Outline each Plasmodium ovale-infected red blood cell.
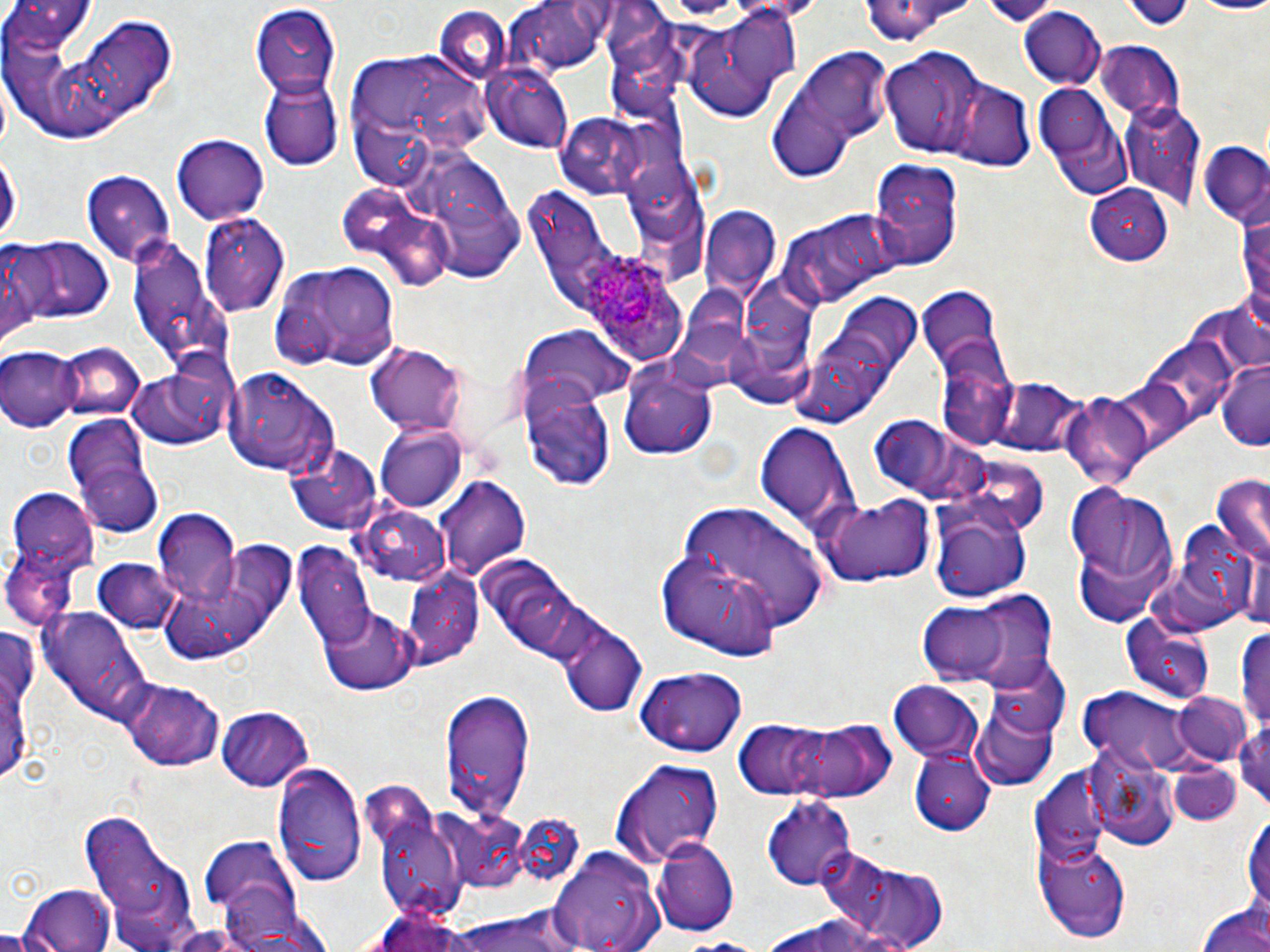
Approximate bounding boxes as (x1, y1, x2, y2) in pixels.
Plasmodium ovale-infected red blood cells: (584, 254, 676, 342).

{
  "slide_level_diagnosis": "Plasmodium ovale",
  "stain": "May-Grünwald-Giemsa",
  "modality": "optical microscopy",
  "field_of_view": "single",
  "preparation": "thin blood smear",
  "uninfected_red_blood_cell_locations": "approximate bounding boxes as (x1, y1, x2, y2) in pixels: (4, 0, 97, 66), (1181, 0, 1270, 16), (858, 1, 977, 44), (510, 2, 614, 76), (247, 4, 340, 97), (434, 6, 510, 86), (677, 8, 806, 121), (1017, 9, 1108, 88), (69, 12, 179, 125), (1095, 42, 1183, 123), (766, 45, 894, 180), (882, 47, 993, 159), (340, 50, 495, 185), (484, 67, 573, 154), (258, 73, 341, 169), (1034, 79, 1131, 196), (949, 80, 1035, 171), (1121, 103, 1206, 208), (554, 111, 654, 200), (169, 134, 271, 223), (1199, 144, 1269, 226), (0, 151, 19, 249), (417, 152, 528, 287), (869, 160, 965, 270), (82, 169, 176, 267), (337, 183, 418, 257), (1087, 184, 1175, 265), (1237, 203, 1270, 324), (700, 204, 781, 299), (777, 207, 899, 309), (200, 212, 290, 318), (382, 212, 456, 293), (126, 234, 230, 371), (20, 237, 113, 325), (1, 240, 51, 340), (275, 259, 402, 371), (917, 286, 1006, 381), (835, 291, 921, 373), (520, 328, 635, 412), (57, 341, 146, 423), (368, 342, 468, 437), (1, 345, 80, 431), (934, 350, 1018, 447), (616, 358, 719, 462), (122, 361, 231, 452), (1216, 362, 1270, 452), (226, 366, 340, 479), (986, 374, 1089, 458), (518, 376, 618, 491), (1059, 391, 1157, 489), (61, 413, 153, 513), (755, 422, 860, 534), (374, 425, 466, 513), (284, 440, 384, 535), (72, 448, 163, 537), (1209, 474, 1270, 568), (437, 475, 530, 579), (1066, 480, 1182, 624), (9, 490, 97, 569), (813, 495, 936, 587), (929, 500, 1034, 606), (671, 502, 830, 641), (356, 505, 453, 589), (151, 512, 242, 606), (163, 539, 298, 664), (5, 545, 81, 630), (295, 547, 372, 648), (94, 559, 180, 635), (401, 566, 484, 672), (965, 593, 1057, 695), (916, 602, 1010, 682), (39, 607, 152, 727), (318, 607, 417, 695), (1121, 615, 1218, 702), (1239, 618, 1270, 734), (557, 621, 647, 716), (985, 657, 1068, 744), (631, 666, 750, 754), (122, 679, 225, 770), (889, 680, 985, 761), (439, 686, 533, 823), (1078, 687, 1198, 771), (1173, 692, 1254, 766), (971, 697, 1057, 791), (218, 706, 315, 791), (730, 715, 895, 803), (1234, 719, 1269, 813), (1086, 741, 1179, 850), (911, 749, 993, 836), (609, 758, 726, 869), (273, 762, 366, 888), (1034, 768, 1110, 865), (758, 795, 858, 892), (78, 806, 199, 952), (375, 807, 467, 925), (1243, 807, 1269, 923), (441, 808, 533, 893), (200, 839, 300, 921), (651, 839, 737, 938), (1036, 839, 1132, 941), (550, 846, 664, 952), (820, 850, 948, 952), (20, 885, 118, 952), (216, 899, 338, 952), (1196, 900, 1270, 952), (365, 905, 481, 952), (448, 909, 583, 952), (762, 911, 910, 952), (669, 937, 776, 952)",
  "magnification": "1000x",
  "image_size": "1270×952 pixels"
}